Identify the parasite.
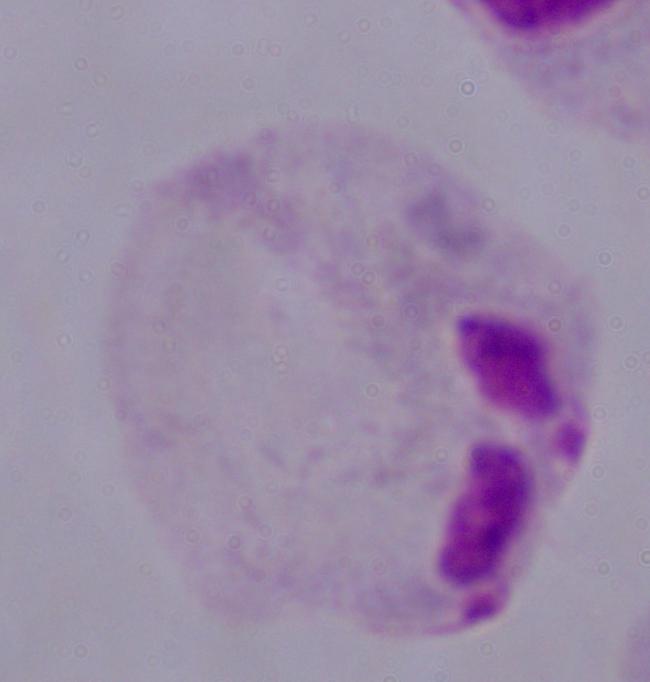
This is a trichomonad.

1000x magnification. Photomicrograph.